State which parasite is depicted.
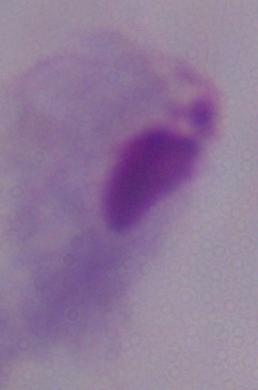
A trichomonad.

Summary:
  - Magnification: 1000x
  - Modality: photomicrograph